Outline each blood parasite and name the species.
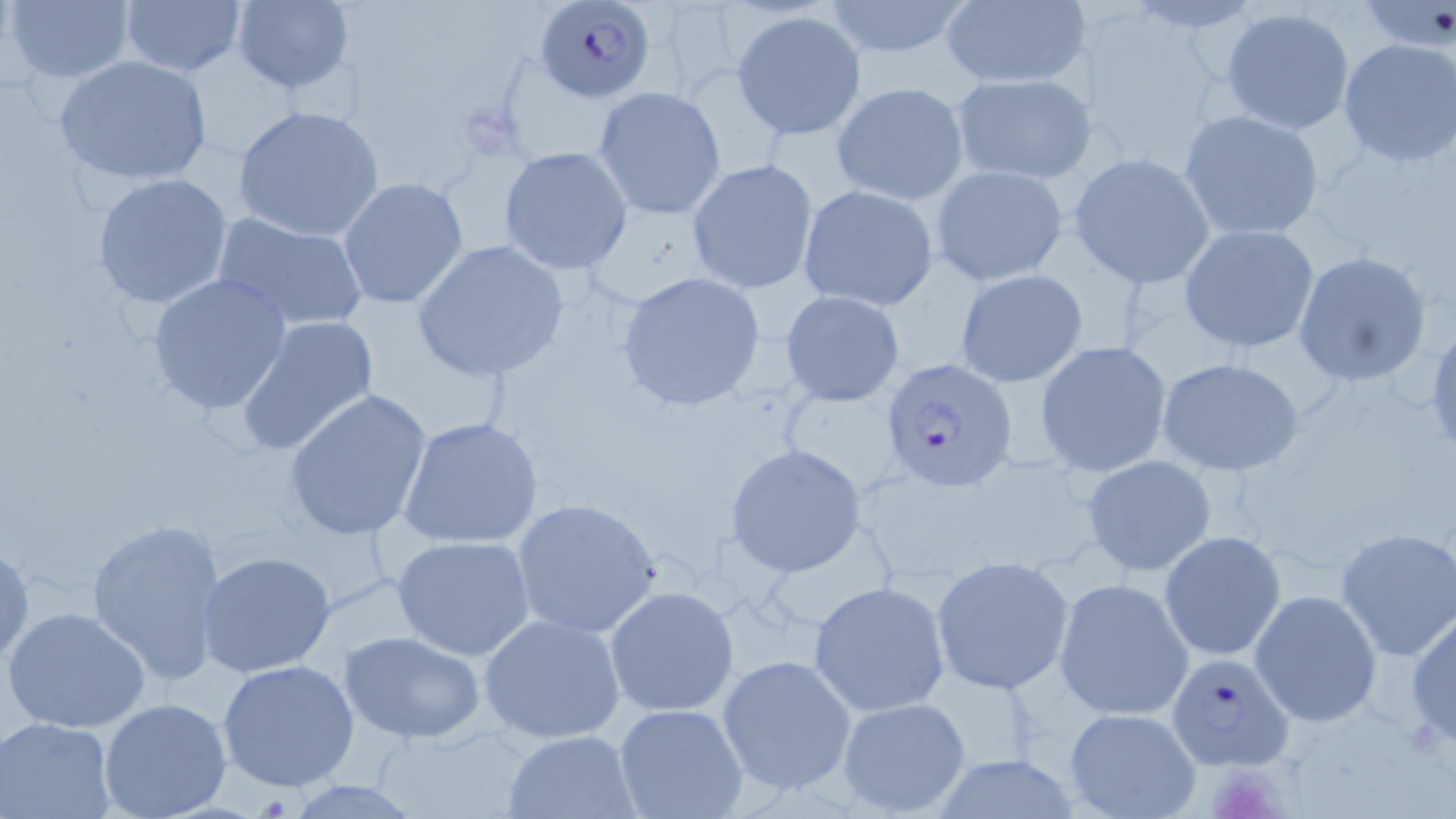

Approximate bounding boxes as [x1, y1, x2, y2] in pixels.
Plasmodium falciparum-infected red blood cells: [535, 0, 655, 103], [880, 357, 1015, 490], [1166, 650, 1297, 771].
No Plasmodium ovale, Plasmodium malariae, Plasmodium vivax, Babesia divergens, or Trypanosoma brucei observed.

Uninfected red blood cell locations: [4, 0, 136, 86], [117, 0, 248, 78], [229, 0, 355, 97], [820, 0, 977, 60], [1359, 1, 1456, 52], [938, 2, 1089, 90], [1220, 6, 1357, 135], [732, 11, 868, 139], [1339, 37, 1456, 168], [53, 54, 214, 188], [950, 71, 1096, 185], [831, 81, 969, 205], [592, 85, 727, 221], [233, 106, 386, 242], [1179, 110, 1325, 240], [499, 147, 631, 274], [1069, 154, 1215, 285], [687, 159, 818, 294], [931, 164, 1068, 286], [92, 172, 234, 310], [338, 176, 470, 310], [797, 185, 939, 313], [210, 210, 369, 333], [1179, 223, 1320, 353], [411, 240, 570, 384], [1293, 250, 1433, 387], [953, 268, 1088, 388], [615, 270, 769, 413], [146, 273, 295, 416], [779, 289, 906, 407], [235, 315, 380, 456], [1033, 341, 1173, 477], [1155, 357, 1304, 477], [283, 389, 432, 542], [398, 415, 543, 549], [724, 445, 867, 577], [1080, 456, 1219, 577], [510, 497, 664, 639], [85, 516, 228, 685], [1335, 527, 1456, 661], [1159, 530, 1287, 661], [393, 535, 534, 661], [0, 544, 32, 666], [197, 551, 337, 678], [930, 556, 1076, 695], [1054, 577, 1194, 721], [809, 580, 951, 715], [605, 585, 740, 718], [1248, 589, 1383, 727], [2, 604, 154, 735], [1408, 606, 1456, 746], [478, 612, 626, 745], [340, 632, 487, 744], [716, 654, 860, 797], [218, 660, 362, 793], [97, 696, 234, 819], [835, 696, 971, 818], [614, 703, 750, 819], [1063, 705, 1202, 818], [0, 717, 116, 818], [503, 729, 638, 817]. Slide-level diagnosis: Plasmodium falciparum. May-Grünwald-Giemsa stain. Thin blood smear. Light microscopy. Captured at 1000x magnification. One field of a larger specimen. Image is 1456×819 pixels.